State the blood parasite species.
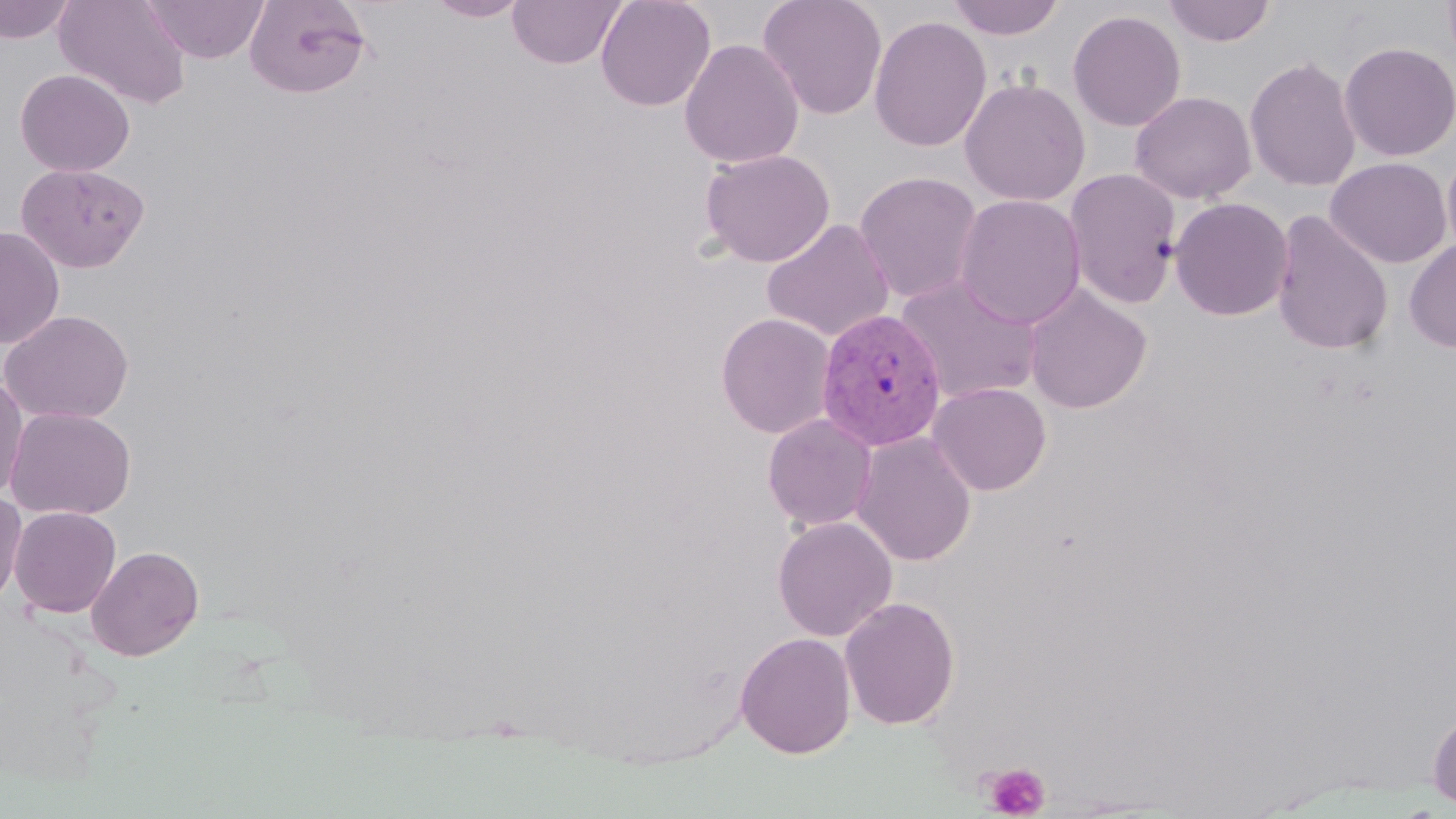
Plasmodium vivax.

Approximate bounding boxes as named x1/y1/x2/y2 corners in pixels. Platelet locations: (x1=983, y1=763, x2=1050, y2=818). Uninfected red blood cell locations: (x1=53, y1=0, x2=192, y2=109), (x1=143, y1=0, x2=269, y2=63), (x1=425, y1=0, x2=531, y2=21), (x1=507, y1=0, x2=627, y2=69), (x1=595, y1=0, x2=717, y2=112), (x1=758, y1=0, x2=887, y2=120), (x1=945, y1=0, x2=1066, y2=41), (x1=1162, y1=0, x2=1276, y2=47), (x1=0, y1=1, x2=76, y2=44), (x1=243, y1=1, x2=373, y2=99), (x1=1067, y1=9, x2=1187, y2=132), (x1=868, y1=14, x2=992, y2=153), (x1=679, y1=38, x2=805, y2=169), (x1=1338, y1=41, x2=1456, y2=162), (x1=1244, y1=55, x2=1362, y2=193), (x1=15, y1=68, x2=135, y2=177), (x1=959, y1=77, x2=1091, y2=206), (x1=1129, y1=90, x2=1257, y2=204), (x1=1442, y1=147, x2=1456, y2=263), (x1=699, y1=148, x2=835, y2=268), (x1=1325, y1=157, x2=1452, y2=269), (x1=16, y1=162, x2=149, y2=273), (x1=1064, y1=168, x2=1181, y2=308), (x1=853, y1=170, x2=984, y2=304), (x1=954, y1=193, x2=1086, y2=329), (x1=1169, y1=197, x2=1294, y2=321), (x1=1270, y1=210, x2=1394, y2=355), (x1=761, y1=218, x2=895, y2=342), (x1=0, y1=225, x2=65, y2=349), (x1=1404, y1=239, x2=1456, y2=353), (x1=894, y1=275, x2=1045, y2=404), (x1=1022, y1=284, x2=1153, y2=414), (x1=0, y1=309, x2=135, y2=425), (x1=715, y1=313, x2=836, y2=438), (x1=0, y1=374, x2=28, y2=503), (x1=927, y1=382, x2=1052, y2=496), (x1=5, y1=406, x2=136, y2=520), (x1=762, y1=413, x2=878, y2=531), (x1=851, y1=431, x2=977, y2=566), (x1=0, y1=492, x2=27, y2=610), (x1=9, y1=506, x2=122, y2=617), (x1=772, y1=515, x2=897, y2=642), (x1=86, y1=545, x2=204, y2=661), (x1=840, y1=596, x2=960, y2=731), (x1=736, y1=631, x2=856, y2=759), (x1=1427, y1=710, x2=1456, y2=809). Plasmodium vivax-infected red blood cell locations: (x1=817, y1=307, x2=947, y2=450). Light microscopy. May-Grünwald-Giemsa stain. One field of a larger specimen. 1000x magnification. Image is 1456×819 pixels. Thin blood film.